Assess this cell for malaria.
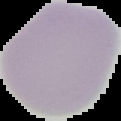

It is uninfected.

Summary:
  - Image type: cell region segmented out of the field of view; surrounding area masked to black
  - Preparation: thin blood smear
  - Image size: 121×121 pixels